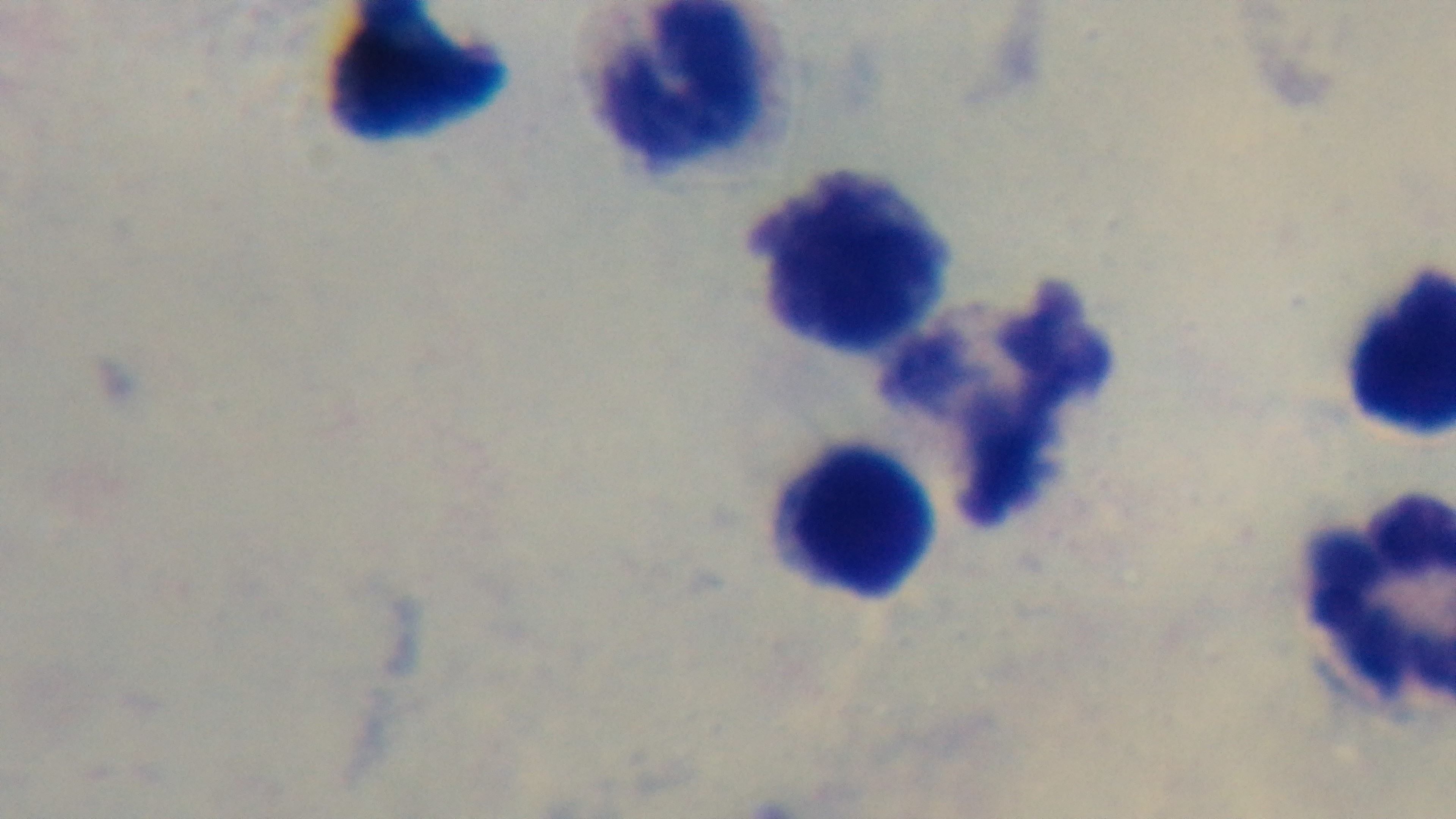

objective = 100x oil immersion
malaria status = negative
stain = Giemsa
modality = light microscopy
field of view = single
capture = mounted 4K digital camera
preparation = thick